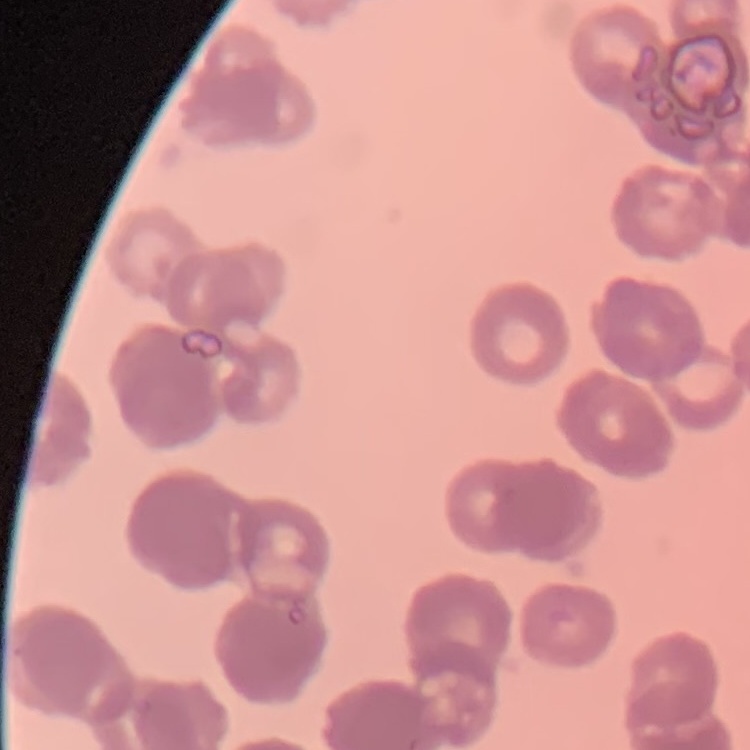

red blood cell morphology = rouleaux formation
preparation = thin blood film
image type = one tile cut from a larger photomicrograph
stain = Field's or Giemsa